State which cell type is depicted.
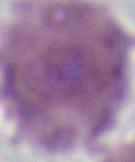

This is an erythrocyte.

Photomicrograph. Captured at 1000x magnification.